Classify this cell by malaria status.
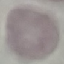

It is uninfected.

Summary:
  - Capture: smartphone through the microscope eyepiece
  - Stain: Giemsa
  - Preparation: thin blood smear
  - Image type: cell patch, automatically extracted from a larger field of view and resized to 64 × 64 pixels